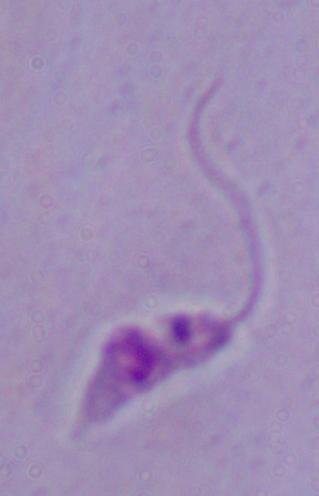
identification = Leishmania
magnification = 1000x
modality = micrograph